Assess this cell for malaria.
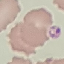
Uninfected.

Photographed with a smartphone camera at the microscope eyepiece. Cell patch, automatically extracted from a larger field of view and resized to 64 × 64 pixels. Thin smear of blood. Giemsa stain.